Classify this cell by malaria status.
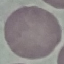

Uninfected.

Summary:
  - Capture: smartphone through the microscope eyepiece
  - Preparation: thin smear
  - Image type: cell patch, automatically extracted from a larger field of view and resized to 64 × 64 pixels
  - Stain: Giemsa